Classify this cell by malaria status.
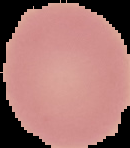

It is uninfected.

Cell region segmented out of the field of view; the surrounding area is masked to black. From a thin blood smear. Image is 130×148 pixels.